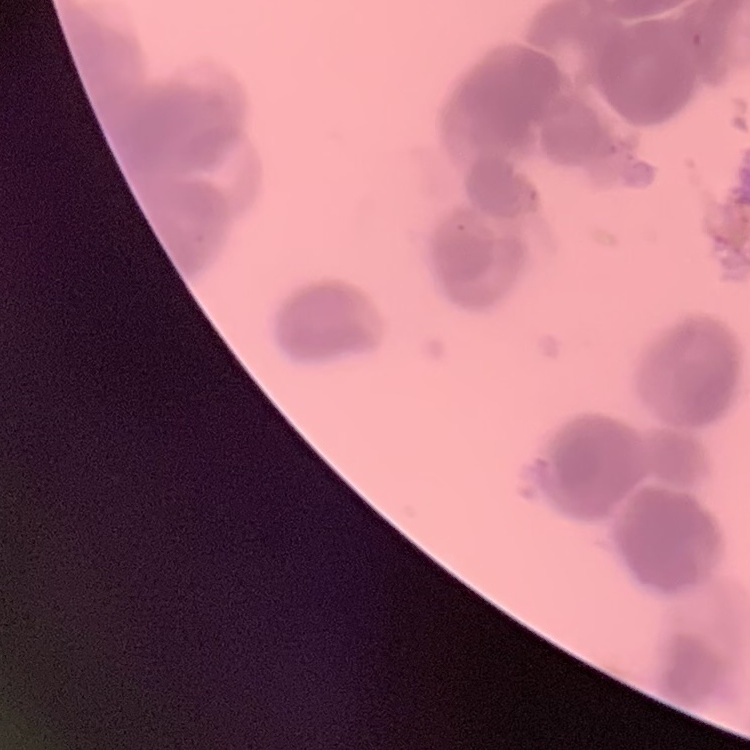

{
  "red_blood_cell_morphology": "rouleaux formation",
  "preparation": "thin blood film",
  "stain": "Field's or Giemsa",
  "image_type": "square crop of a larger photomicrograph"
}